Assess this cell for malaria.
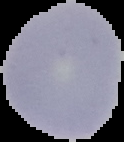
It is uninfected.

From a thin blood film. The area outside the segmented cell region is set to black. Image is 124×142 pixels.